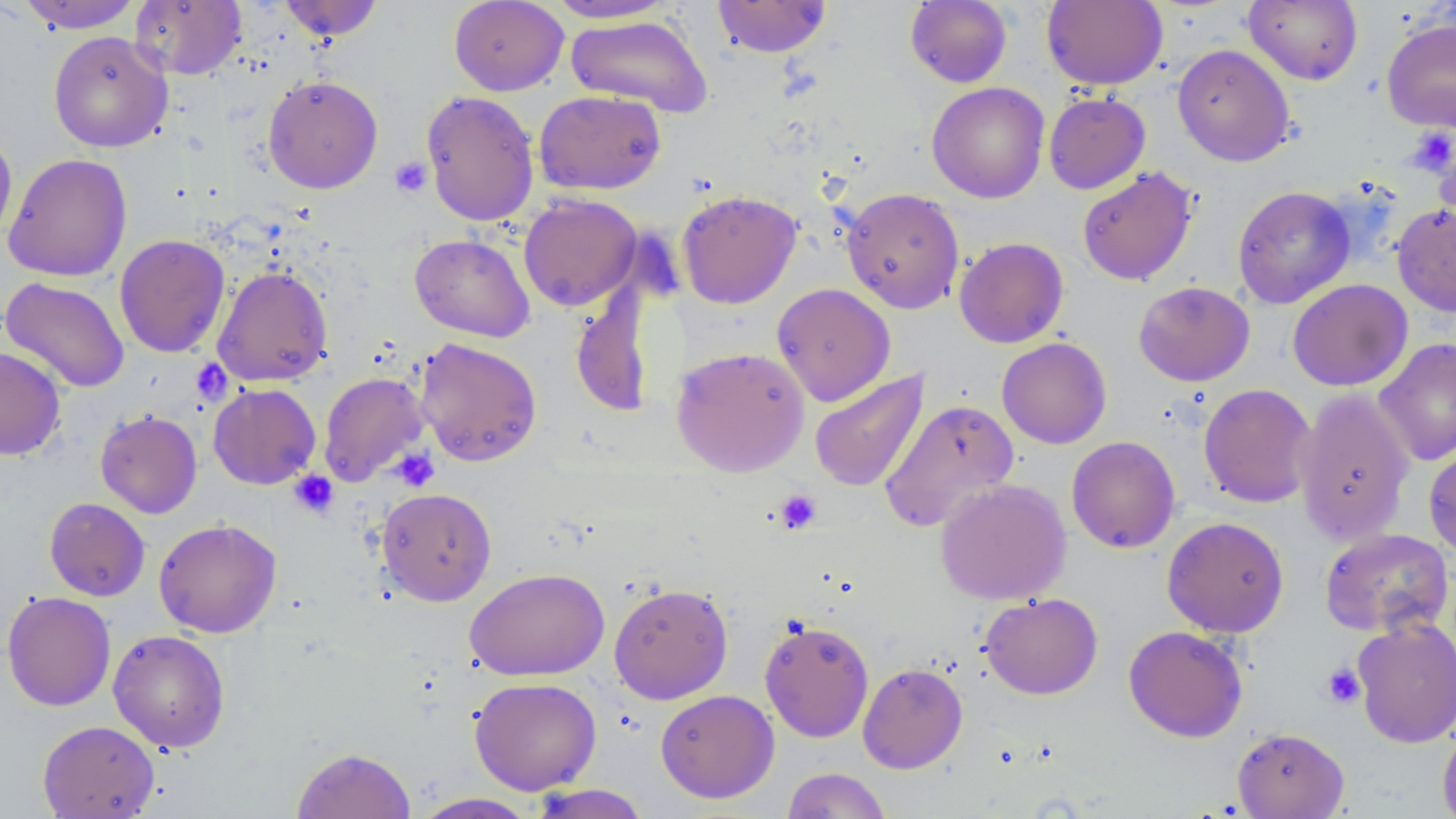

Approximate bounding boxes as (x1, y1, x2, y2) in pixels. Uninfected red blood cell locations: (130, 0, 246, 80), (278, 0, 384, 41), (544, 0, 678, 23), (712, 0, 831, 58), (905, 0, 1013, 88), (1243, 0, 1363, 85), (17, 1, 142, 33), (449, 1, 569, 95), (1042, 1, 1167, 90), (565, 15, 713, 117), (1381, 18, 1456, 132), (48, 31, 173, 153), (1172, 43, 1296, 167), (262, 75, 383, 193), (926, 82, 1050, 203), (421, 89, 540, 227), (533, 90, 666, 195), (1043, 92, 1151, 194), (0, 122, 18, 247), (3, 152, 132, 281), (1077, 166, 1198, 285), (1232, 185, 1356, 308), (841, 187, 965, 314), (677, 190, 802, 308), (519, 194, 642, 311), (1392, 203, 1456, 317), (114, 233, 231, 358), (409, 233, 535, 342), (954, 237, 1069, 348), (212, 265, 333, 387), (0, 277, 130, 393), (1287, 279, 1413, 391), (1133, 281, 1255, 386), (771, 283, 895, 406), (570, 285, 655, 420), (414, 337, 543, 467), (997, 337, 1112, 448), (1373, 338, 1456, 467), (671, 346, 810, 477), (0, 347, 66, 460), (810, 369, 929, 492), (318, 371, 430, 487), (208, 383, 321, 490), (1198, 383, 1317, 508), (1294, 388, 1415, 546), (879, 399, 1020, 531), (95, 410, 202, 518), (1066, 436, 1181, 553), (1423, 443, 1456, 561), (935, 478, 1071, 605), (376, 487, 497, 606), (44, 497, 150, 601), (1162, 516, 1290, 637), (153, 518, 282, 638), (1319, 528, 1454, 638), (465, 567, 610, 681), (608, 582, 733, 704), (2, 590, 116, 712), (979, 592, 1103, 699), (1351, 616, 1456, 748), (759, 618, 875, 742), (1123, 625, 1248, 742), (108, 629, 230, 753), (858, 662, 968, 773), (469, 677, 601, 795), (655, 689, 779, 803), (37, 720, 160, 818), (1437, 720, 1456, 819), (1232, 726, 1349, 818), (291, 746, 416, 819), (781, 767, 892, 818), (527, 784, 650, 818), (411, 793, 538, 819). Platelet locations: (1407, 127, 1455, 176), (389, 156, 433, 198), (390, 447, 440, 491), (289, 470, 339, 519), (775, 489, 821, 534), (1320, 663, 1365, 708). Slide-level diagnosis: no evidence of blood parasites. May-Grünwald-Giemsa stain. Image is 1456×819 pixels. 1000x magnification. Optical microscopy. Single field of view. Thin blood smear.